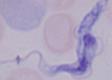

modality: photomicrograph
identification: trypanosome
magnification: 1000x